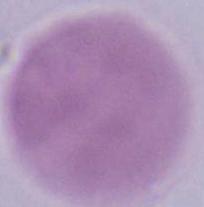

Summary:
  - Magnification: 1000x
  - Identification: red blood cell
  - Modality: photomicrograph